Name the parasite shown.
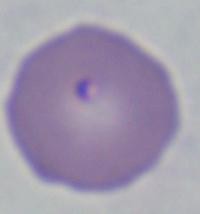

Babesia.

magnification = 1000x
modality = micrograph